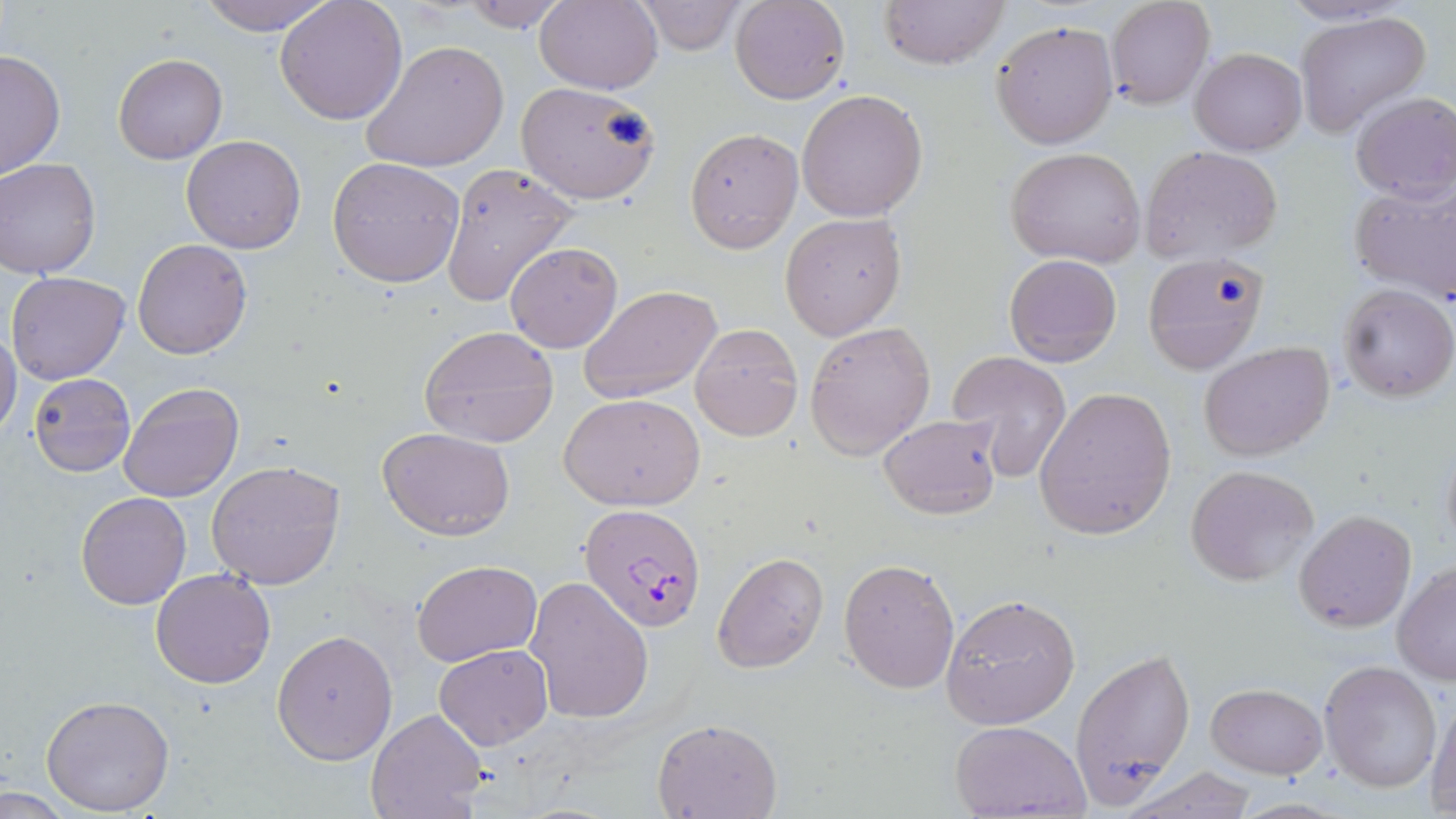 Approximate bounding boxes as named x1/y1/x2/y2 corners in pixels. Uninfected red blood cell locations: (x1=197, y1=0, x2=332, y2=36), (x1=535, y1=0, x2=662, y2=93), (x1=728, y1=0, x2=850, y2=104), (x1=878, y1=0, x2=1010, y2=69), (x1=275, y1=1, x2=405, y2=124), (x1=457, y1=1, x2=572, y2=31), (x1=635, y1=1, x2=745, y2=54), (x1=1106, y1=1, x2=1215, y2=109), (x1=1295, y1=11, x2=1431, y2=138), (x1=992, y1=20, x2=1119, y2=148), (x1=361, y1=40, x2=508, y2=175), (x1=1189, y1=47, x2=1307, y2=155), (x1=0, y1=49, x2=66, y2=177), (x1=113, y1=53, x2=227, y2=164), (x1=514, y1=81, x2=661, y2=206), (x1=795, y1=89, x2=929, y2=222), (x1=1350, y1=91, x2=1456, y2=204), (x1=685, y1=128, x2=803, y2=252), (x1=182, y1=134, x2=306, y2=255), (x1=1006, y1=146, x2=1147, y2=267), (x1=1142, y1=147, x2=1280, y2=258), (x1=328, y1=156, x2=466, y2=288), (x1=0, y1=158, x2=100, y2=279), (x1=439, y1=163, x2=575, y2=309), (x1=1349, y1=180, x2=1456, y2=302), (x1=779, y1=212, x2=907, y2=340), (x1=132, y1=238, x2=253, y2=358), (x1=505, y1=243, x2=623, y2=353), (x1=1004, y1=254, x2=1122, y2=369), (x1=1141, y1=254, x2=1269, y2=374), (x1=6, y1=272, x2=130, y2=386), (x1=1337, y1=282, x2=1455, y2=403), (x1=580, y1=285, x2=721, y2=403), (x1=803, y1=321, x2=936, y2=459), (x1=689, y1=324, x2=802, y2=442), (x1=419, y1=325, x2=560, y2=447), (x1=0, y1=330, x2=21, y2=443), (x1=1198, y1=342, x2=1335, y2=462), (x1=945, y1=349, x2=1075, y2=479), (x1=28, y1=373, x2=136, y2=477), (x1=118, y1=380, x2=244, y2=503), (x1=1034, y1=387, x2=1176, y2=540), (x1=558, y1=392, x2=705, y2=511), (x1=877, y1=412, x2=1002, y2=521), (x1=377, y1=426, x2=516, y2=539), (x1=1439, y1=438, x2=1456, y2=561), (x1=207, y1=459, x2=345, y2=591), (x1=1186, y1=463, x2=1320, y2=587), (x1=76, y1=492, x2=191, y2=610), (x1=1293, y1=510, x2=1416, y2=631), (x1=712, y1=552, x2=829, y2=674), (x1=839, y1=557, x2=961, y2=693), (x1=411, y1=559, x2=542, y2=667), (x1=1393, y1=564, x2=1456, y2=684), (x1=150, y1=569, x2=276, y2=689), (x1=526, y1=577, x2=654, y2=723), (x1=940, y1=594, x2=1080, y2=729), (x1=272, y1=628, x2=398, y2=763), (x1=433, y1=643, x2=552, y2=748), (x1=1070, y1=649, x2=1197, y2=799), (x1=1319, y1=660, x2=1442, y2=793), (x1=1206, y1=683, x2=1326, y2=778), (x1=41, y1=694, x2=174, y2=815), (x1=1427, y1=699, x2=1456, y2=817), (x1=366, y1=708, x2=490, y2=819), (x1=652, y1=718, x2=782, y2=818), (x1=950, y1=720, x2=1090, y2=818), (x1=1121, y1=767, x2=1259, y2=819). Plasmodium falciparum-infected red blood cell locations: (x1=580, y1=504, x2=708, y2=635). Slide-level diagnosis: Plasmodium falciparum. May-Grünwald-Giemsa stain. Image is 1456×819 pixels. Optical microscopy. Single field of view. Thin blood smear. Captured at 1000x magnification.